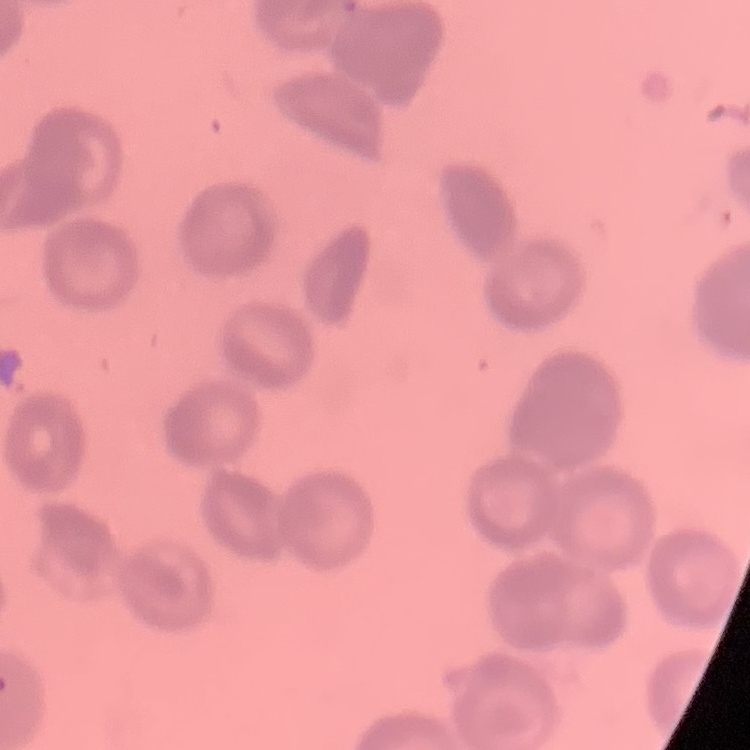

Summary:
  - Erythrocyte morphology: rouleaux formation
  - Preparation: thin peripheral smear
  - Stain: Field's or Giemsa
  - Image type: one tile cut from a larger photomicrograph